Locate every Plasmodium parasite.
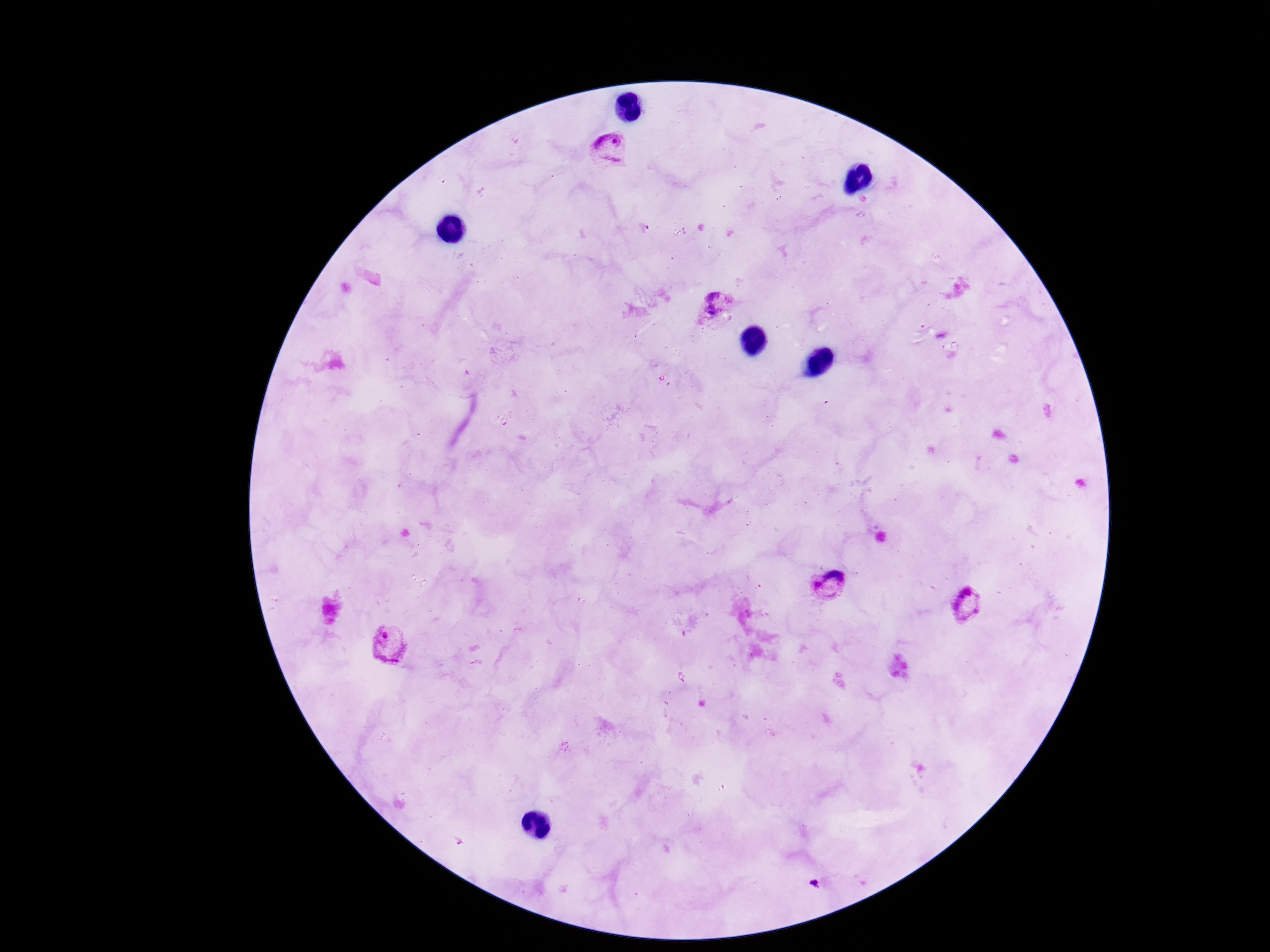
Approximate centers as (x, y) in pixels.
Plasmodium parasites: (608, 147), (719, 308), (828, 586), (968, 604), (387, 643), (815, 883).

magnification = 100x
field of view = single
patient malaria status = infected
capture = smartphone camera through the microscope eyepiece
stain = Giemsa
preparation = thick blood film
image size = 1270×952 pixels